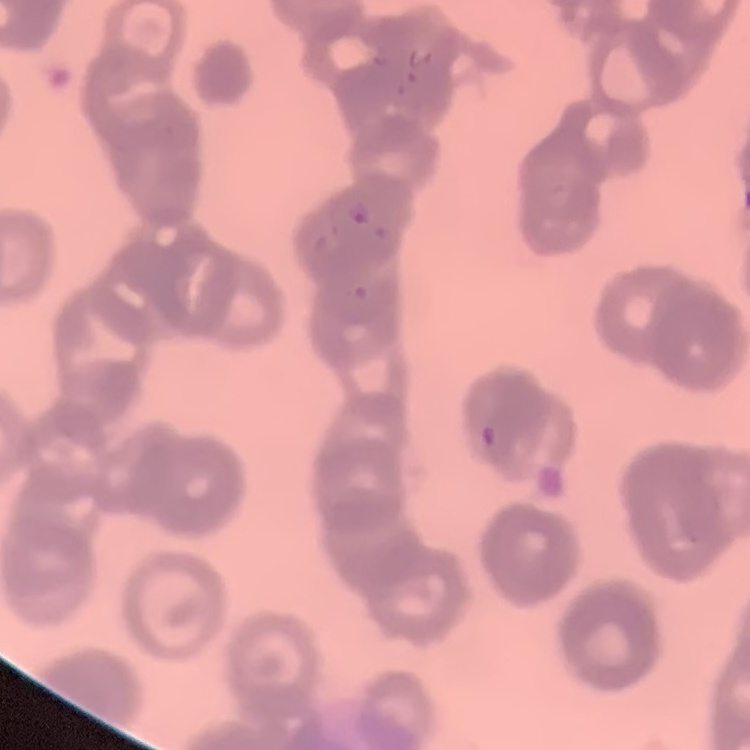
red_blood_cell_morphology: rouleaux formation
image_type: square crop of a larger photomicrograph
preparation: thin blood smear
stain: Field's or Giemsa